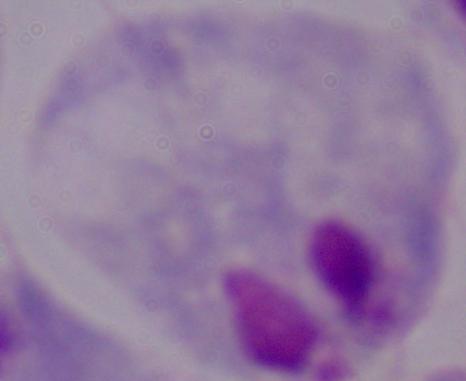 A trichomonad is shown. Captured at 1000x magnification. Photomicrograph.